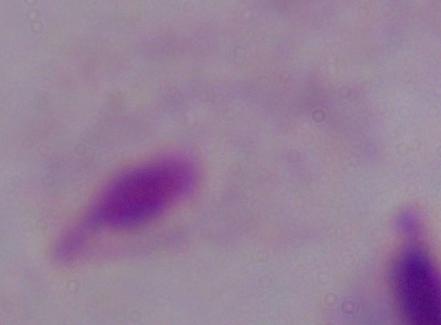

Summary:
  - Identification: trichomonad
  - Modality: photomicrograph
  - Magnification: 1000x